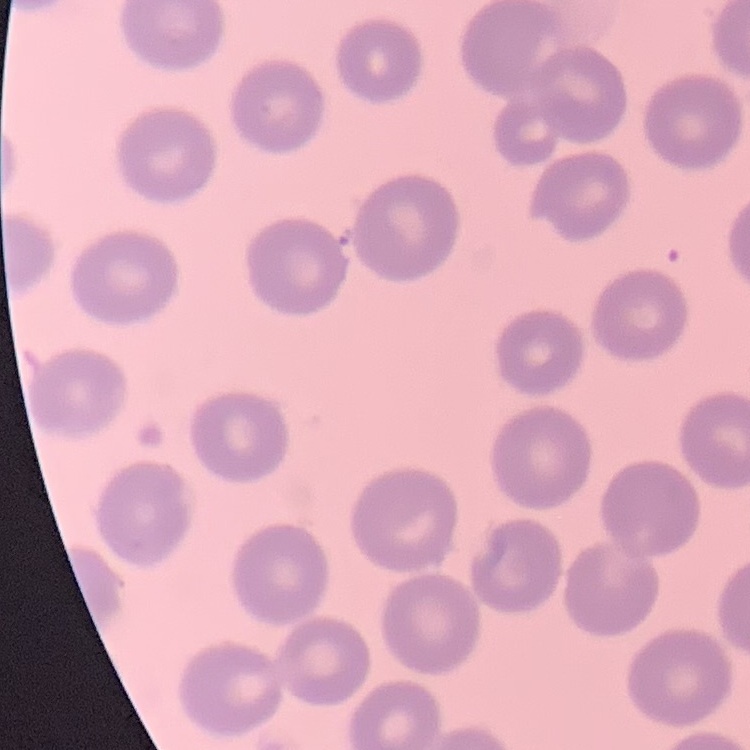

Summary:
  - Red blood cell morphology: no rouleaux formation
  - Image type: one tile cut from a larger photomicrograph
  - Preparation: thin peripheral smear
  - Stain: Field's or Giemsa